Comment on the morphology of the red blood cells.
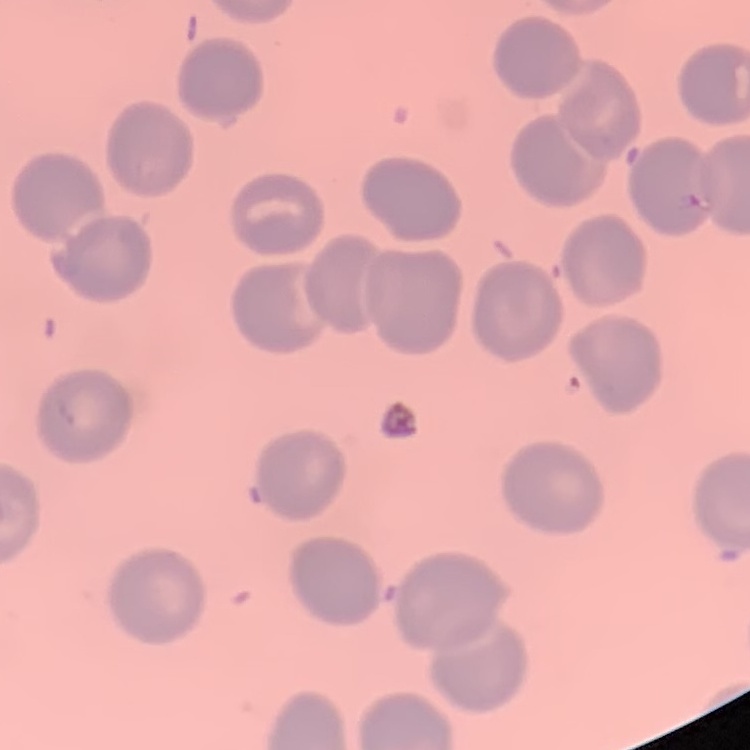
No rouleaux formation.

Summary:
  - Image type: one tile cut from a larger photomicrograph
  - Preparation: thin peripheral smear
  - Stain: Field's or Giemsa